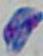

magnification = 1000x
modality = photomicrograph
identification = Toxoplasma gondii